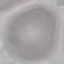

result = no malaria parasites seen
stain = Giemsa
capture = smartphone through the microscope eyepiece
preparation = thin blood film
image type = cell patch, automatically extracted from a larger field of view and resized to 64 × 64 pixels